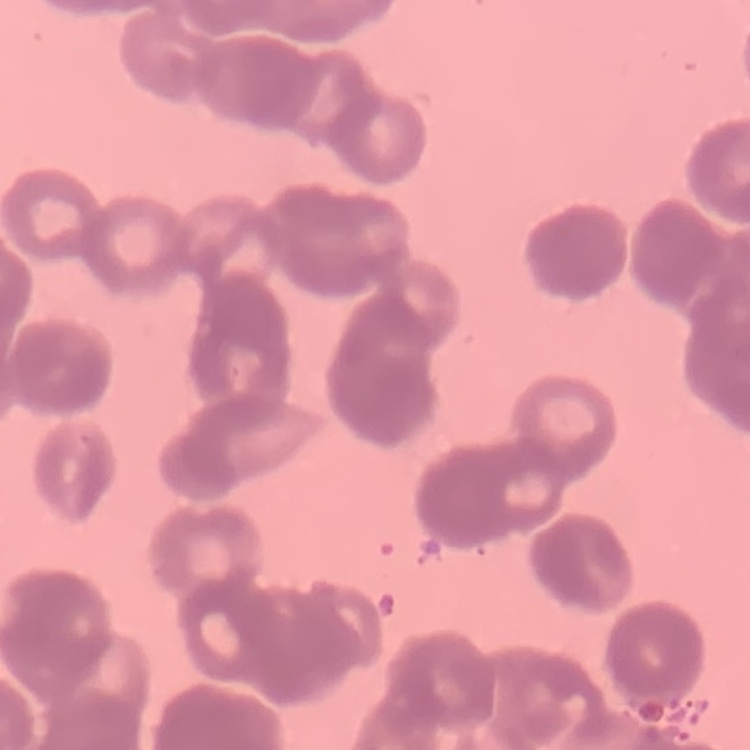 The red blood cells exhibit rouleaux formation. One tile cut from a larger photomicrograph. Thin peripheral smear. Stained with either Field's or Giemsa.